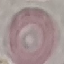
result = negative for malaria parasites
stain = Giemsa
capture = smartphone through the microscope eyepiece
image type = automatically extracted cell patch, resized to 64 × 64 pixels
preparation = thin blood film